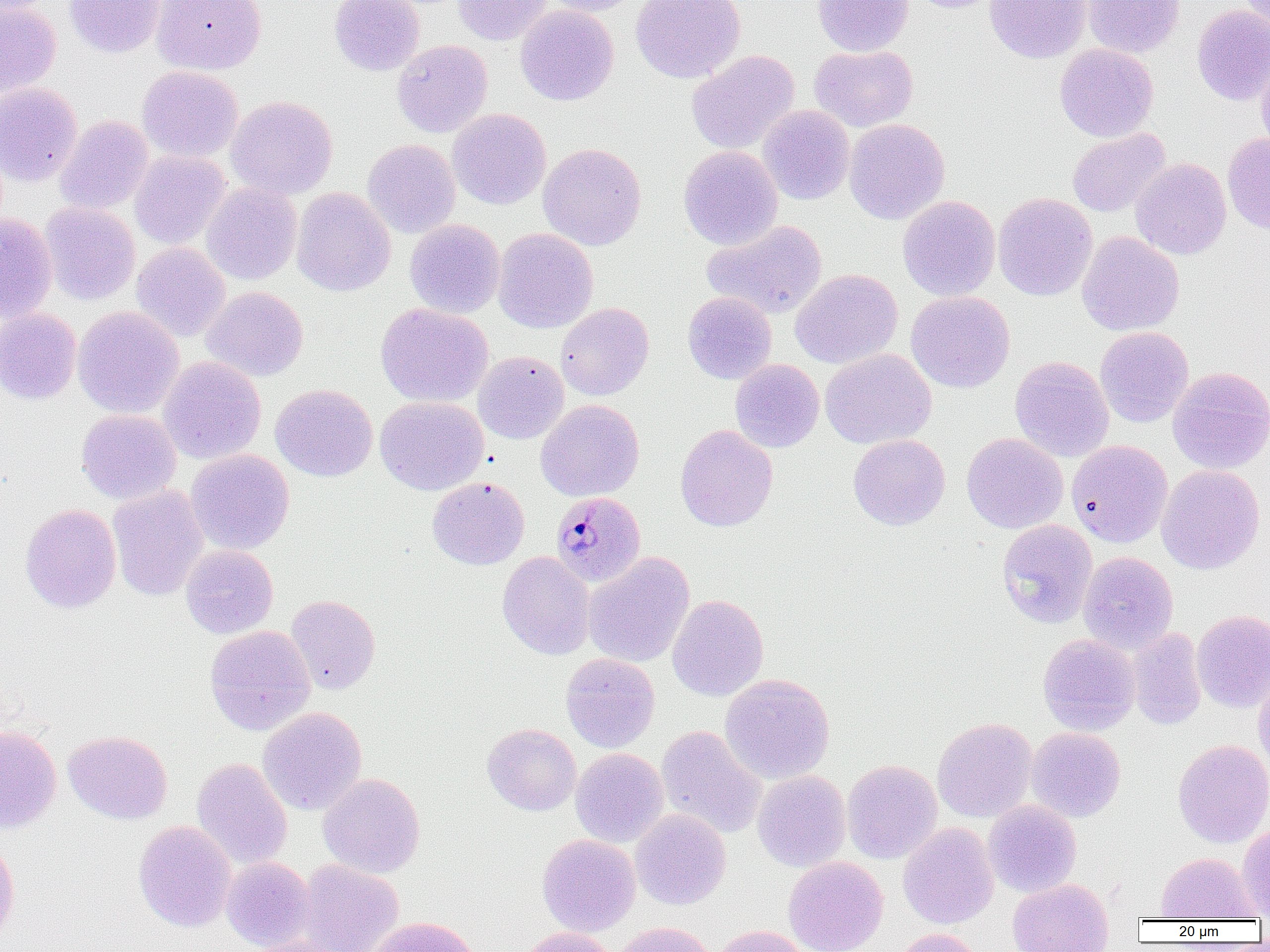

Summary:
  - Coordinate format: approximate bounding boxes as [x1, y1, x2, y2] in pixels
  - Uninfected red blood cell locations: [64, 0, 164, 58], [151, 0, 267, 75], [329, 0, 425, 76], [453, 0, 554, 45], [542, 0, 643, 16], [630, 0, 746, 84], [812, 0, 913, 56], [906, 0, 1006, 13], [984, 0, 1092, 63], [1082, 0, 1185, 58], [1236, 0, 1270, 31], [0, 2, 61, 97], [515, 4, 619, 106], [1192, 5, 1270, 106], [392, 40, 492, 138], [1055, 43, 1159, 142], [809, 45, 918, 132], [686, 50, 800, 154], [1256, 52, 1270, 158], [137, 66, 243, 163], [0, 83, 83, 186], [226, 95, 338, 200], [758, 105, 855, 205], [448, 108, 551, 209], [55, 115, 154, 214], [844, 118, 950, 224], [1067, 128, 1169, 218], [1222, 133, 1270, 234], [362, 138, 461, 238], [538, 143, 647, 250], [678, 145, 783, 250], [130, 150, 231, 249], [1131, 158, 1231, 260], [201, 182, 301, 285], [291, 187, 395, 297], [993, 192, 1097, 301], [898, 195, 1000, 301], [40, 202, 140, 305], [0, 213, 57, 322], [405, 219, 505, 317], [702, 220, 828, 320], [492, 228, 598, 333], [1077, 231, 1184, 336], [131, 242, 231, 342], [790, 269, 903, 368], [201, 286, 309, 381], [906, 291, 1015, 393], [683, 292, 777, 384], [555, 302, 655, 401], [375, 303, 493, 408], [73, 306, 184, 419], [0, 307, 82, 404], [1095, 326, 1194, 427], [820, 348, 936, 449], [473, 351, 569, 444], [1010, 356, 1114, 462], [158, 357, 266, 464], [730, 359, 824, 452], [1167, 366, 1270, 474], [270, 384, 378, 481], [375, 396, 488, 495], [535, 399, 644, 502], [76, 409, 181, 505], [675, 424, 778, 532], [961, 432, 1068, 534], [848, 434, 950, 530], [1067, 440, 1173, 547], [185, 449, 294, 554], [1156, 464, 1265, 575], [427, 477, 530, 569], [107, 486, 209, 601], [20, 503, 121, 614], [996, 519, 1098, 628], [180, 544, 278, 639], [497, 551, 596, 660], [1078, 551, 1179, 655], [583, 552, 695, 668], [667, 594, 769, 701], [286, 595, 380, 694], [1191, 609, 1270, 712], [205, 625, 316, 735], [1127, 628, 1207, 729], [1037, 633, 1140, 735], [560, 653, 660, 752], [1253, 666, 1270, 772], [719, 674, 835, 785], [258, 706, 367, 816], [932, 717, 1037, 822], [0, 723, 62, 834], [482, 723, 581, 815], [656, 725, 768, 840], [1027, 727, 1126, 822], [63, 730, 172, 824], [1172, 739, 1270, 847], [570, 748, 669, 847], [191, 757, 292, 870], [842, 759, 942, 864], [752, 770, 851, 872], [318, 773, 425, 878], [982, 800, 1081, 897], [630, 809, 731, 909], [133, 820, 237, 932], [1237, 822, 1270, 918], [898, 823, 999, 929], [0, 834, 20, 946], [537, 834, 641, 936], [1156, 852, 1259, 920], [222, 856, 315, 951], [783, 856, 888, 952], [296, 859, 404, 952], [1007, 878, 1113, 952], [364, 917, 481, 952], [612, 921, 715, 952], [711, 925, 814, 952], [517, 927, 619, 952], [890, 928, 985, 952], [242, 936, 352, 952]
  - Plasmodium malariae-infected red blood cell locations: [551, 491, 646, 586]
  - Slide-level diagnosis: Plasmodium malariae
  - Modality: light microscopy
  - Magnification: 1000x
  - Field of view: one of a larger specimen
  - Preparation: thin blood smear
  - Image size: 1270×952 pixels